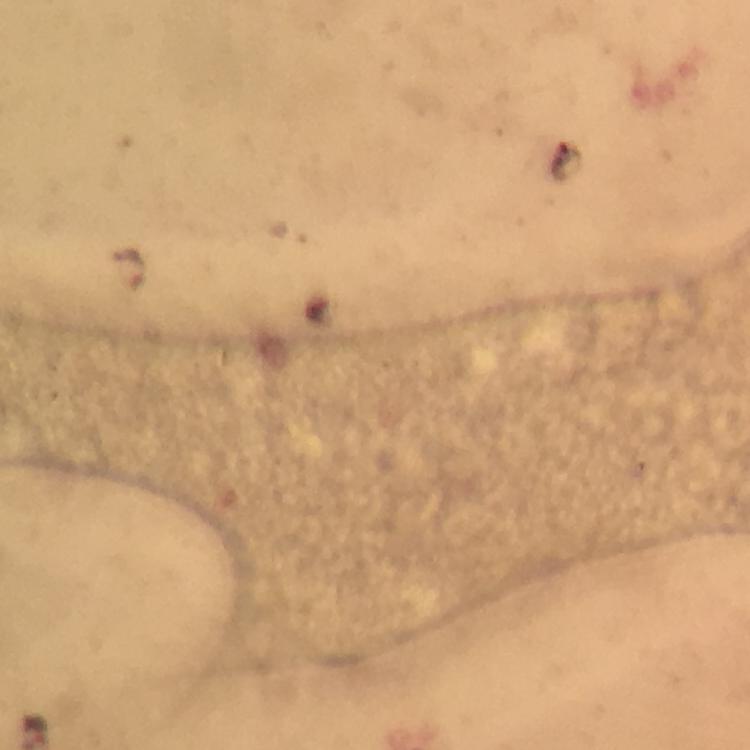
Approximate centers as [x, y] in pixels. Malaria parasite locations: [129, 269]. Thick smear. Image is 750×750 pixels. At 100x magnification. Giemsa stain. Cropped region of a single field of view. Immersion oil was used. Smartphone photograph taken through a microscope. From a malaria diagnostic workup.